Comment on the morphology of the erythrocytes.
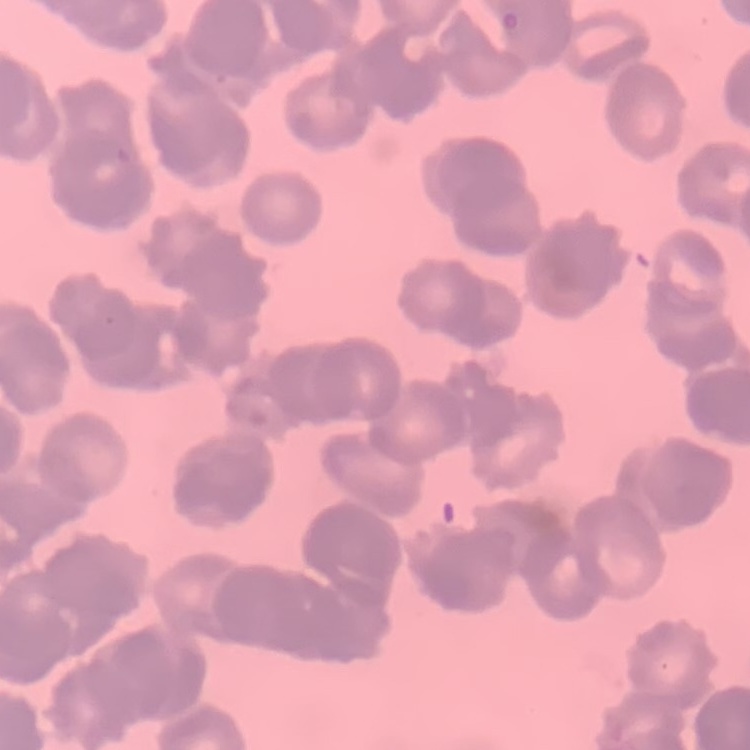
Rouleaux formation.

preparation = thin peripheral smear
image type = one tile cut from a larger photomicrograph
stain = Field's or Giemsa